Classify this cell by malaria status.
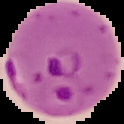
It is parasitized.

preparation: thin blood film
image_size: 124×124 pixels
image_type: cell region segmented out of the field of view; surrounding area masked to black